Classify this cell by malaria status.
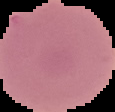
It is uninfected.

Image is 115×112 pixels. From a thin blood film. Cell region segmented out of the field of view; the surrounding area is masked to black.